Assess the background quality.
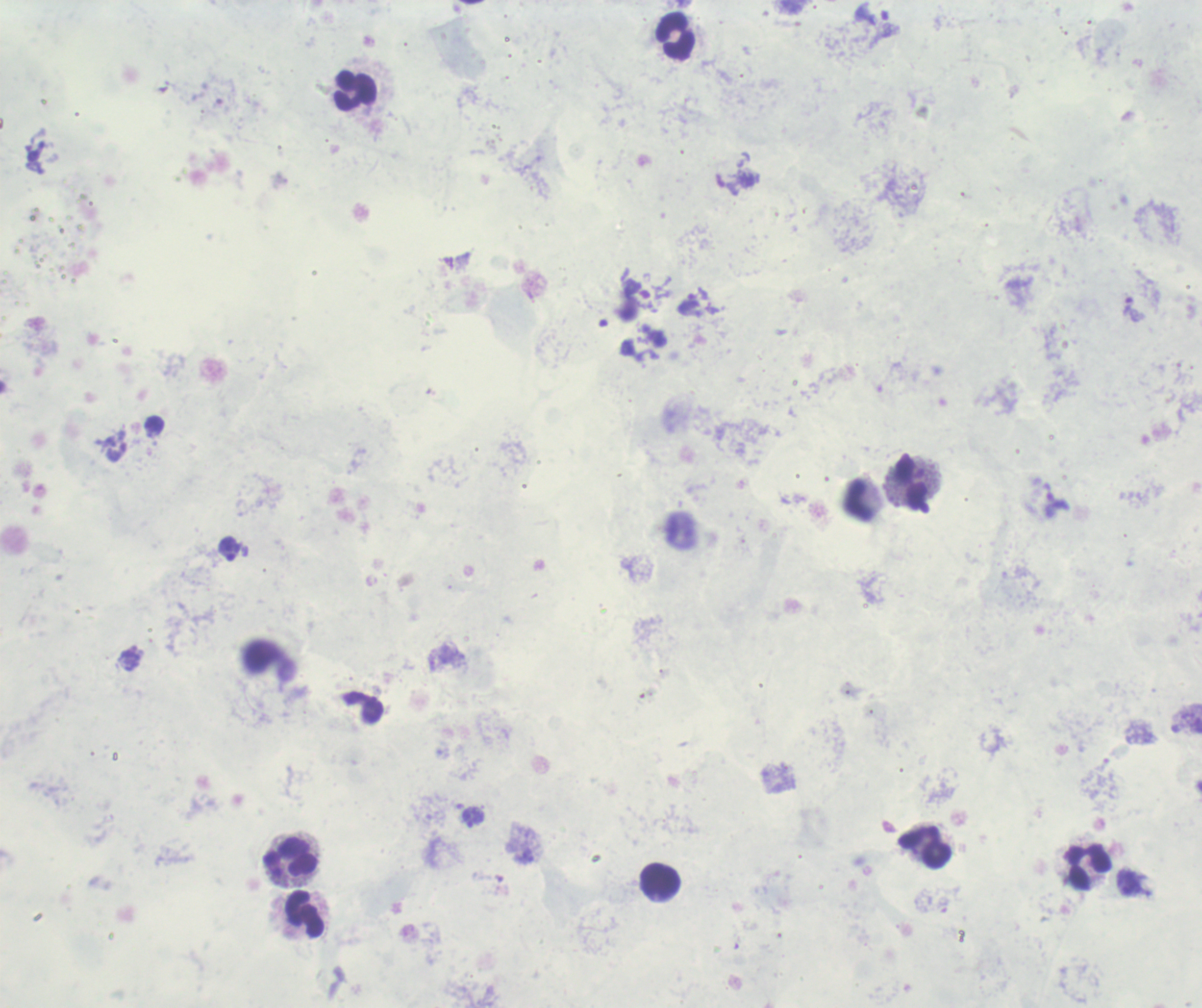

Poor.

Approximate object centers, in pixels from the top-left corner. Trophozoite locations: (x=689, y=305), (x=1133, y=310), (x=1058, y=504), (x=230, y=549), (x=473, y=816). Leukocyte locations: (x=676, y=36), (x=356, y=91), (x=910, y=482), (x=859, y=501), (x=926, y=847), (x=290, y=856), (x=1089, y=869), (x=660, y=880), (x=305, y=915). Image is 1202×1008 pixels. Captured at 100x magnification. Romanowsky stain. Previously used in an actual diagnosis. One field from this slide. Thick blood smear. Result: Plasmodium parasites identified.